Name the parasite shown.
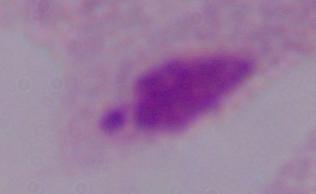

A trichomonad.

{
  "magnification": "1000x",
  "modality": "micrograph"
}